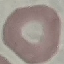
Result: negative for malaria parasites. Thin smear of blood. Automatically extracted cell patch, resized to 64 × 64 pixels. Acquired by smartphone through the microscope eyepiece. Giemsa-stained preparation.